Outline each uninfected red blood cell.
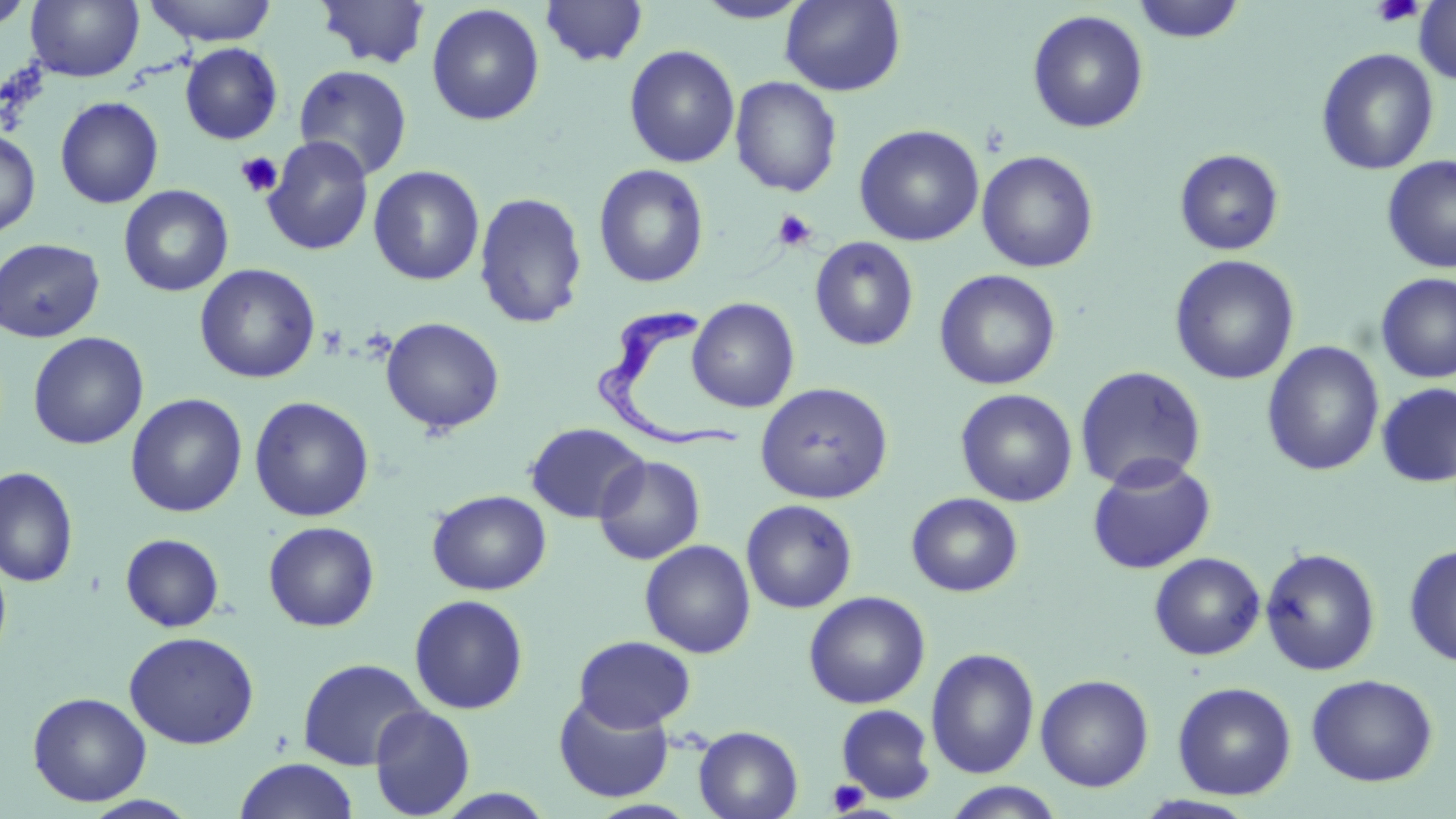
Approximate bounding boxes as (x1, y1, x2, y2) in pixels.
Uninfected red blood cells: (25, 0, 144, 82), (143, 0, 277, 46), (540, 0, 649, 67), (1414, 0, 1456, 84), (1, 1, 36, 32), (315, 1, 432, 69), (694, 1, 812, 24), (780, 1, 906, 96), (1131, 1, 1247, 44), (426, 4, 545, 126), (1027, 9, 1149, 133), (180, 43, 283, 145), (624, 44, 740, 168), (1316, 48, 1439, 175), (293, 64, 413, 181), (730, 76, 842, 197), (55, 96, 164, 208), (854, 124, 984, 246), (0, 129, 40, 238), (262, 135, 373, 256), (1174, 148, 1285, 255), (977, 150, 1099, 273), (1381, 156, 1456, 273), (594, 164, 708, 288), (368, 165, 485, 286), (118, 185, 233, 297), (473, 191, 588, 329), (810, 236, 919, 351), (0, 238, 105, 343), (1169, 254, 1300, 385), (194, 263, 321, 383), (934, 269, 1061, 390), (1374, 272, 1456, 383), (688, 297, 800, 413), (380, 317, 505, 435), (28, 332, 149, 450), (1262, 340, 1385, 477), (1074, 365, 1207, 492), (756, 382, 893, 504), (1376, 382, 1456, 488), (955, 388, 1078, 507), (125, 393, 248, 518), (249, 396, 375, 522), (525, 422, 648, 523), (593, 455, 705, 565), (1086, 455, 1216, 575), (0, 466, 79, 587), (427, 489, 551, 595), (906, 492, 1023, 597), (741, 499, 858, 614), (263, 521, 379, 632), (120, 533, 225, 632), (639, 539, 756, 658), (1403, 544, 1456, 667), (1260, 547, 1381, 675), (0, 549, 12, 669), (1148, 552, 1265, 660), (803, 590, 931, 709), (409, 594, 529, 715), (124, 630, 260, 749), (573, 635, 696, 732), (925, 647, 1040, 779), (297, 657, 429, 770), (1035, 673, 1155, 792), (1306, 673, 1438, 786), (1172, 681, 1297, 800), (27, 691, 151, 806), (553, 693, 675, 803), (835, 703, 938, 805), (369, 704, 476, 818), (693, 725, 803, 819), (233, 758, 360, 819), (942, 782, 1066, 818), (80, 795, 201, 819).

slide-level diagnosis = Trypanosoma brucei
field of view = single
stain = May-Grünwald-Giemsa
modality = light microscopy
preparation = thin blood film
image size = 1456×819 pixels
platelet locations = approximate bounding boxes as (x1, y1, x2, y2) in pixels: (1372, 0, 1424, 27), (235, 151, 283, 198), (771, 210, 817, 252), (827, 779, 868, 815)
Trypanosoma brucei locations = approximate bounding boxes as (x1, y1, x2, y2) in pixels: (595, 304, 748, 460)
magnification = 1000x